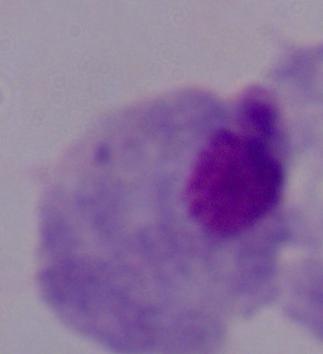
Summary:
  - Identification: trichomonad
  - Modality: photomicrograph
  - Magnification: 1000x